Locate every blood parasite and identify its species.
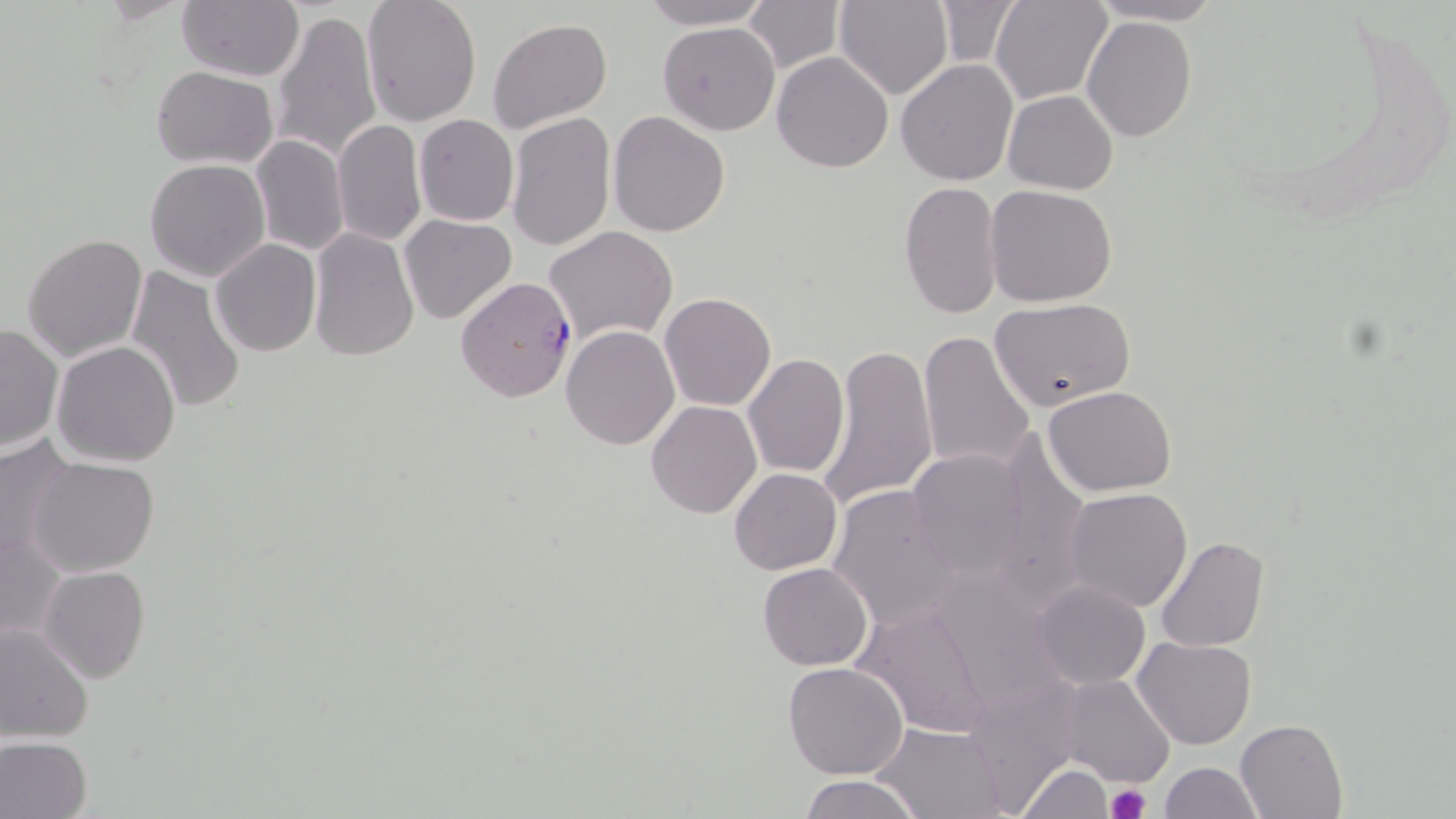
Approximate bounding boxes as (x1,y1)-(x2,y2) corner pairs in pixels.
Plasmodium falciparum-infected red blood cells: (454,276)-(579,405).
No Plasmodium ovale, Plasmodium malariae, Plasmodium vivax, Babesia divergens, or Trypanosoma brucei observed.

Uninfected red blood cell locations: (177,0)-(303,82), (360,0)-(483,127), (635,0)-(773,29), (835,0)-(953,100), (990,0)-(1111,105), (740,1)-(848,76), (934,2)-(1020,67), (1081,2)-(1233,26), (270,8)-(382,165), (1082,15)-(1198,141), (487,17)-(613,135), (658,21)-(780,134), (772,50)-(893,173), (896,59)-(1019,187), (151,66)-(277,167), (1003,90)-(1119,194), (607,111)-(731,237), (506,112)-(615,252), (414,114)-(519,226), (332,117)-(425,249), (249,135)-(349,257), (145,158)-(270,281), (899,180)-(1005,322), (984,184)-(1117,306), (399,214)-(518,325), (544,225)-(679,346), (310,226)-(419,363), (22,233)-(148,362), (209,239)-(321,356), (125,267)-(244,416), (660,291)-(776,411), (990,297)-(1136,412), (0,322)-(63,453), (561,324)-(679,449), (919,330)-(1035,475), (51,341)-(181,466), (817,341)-(938,510), (742,353)-(849,477), (1046,385)-(1176,496), (645,401)-(761,518), (993,430)-(1089,608), (0,434)-(80,566), (905,448)-(1029,581), (27,457)-(159,575), (728,467)-(843,574), (826,484)-(967,632), (1063,487)-(1193,613), (0,527)-(66,642), (1154,536)-(1270,653), (758,562)-(873,670), (39,565)-(151,685), (1031,580)-(1149,690), (854,601)-(996,741), (0,622)-(95,744), (1133,636)-(1257,749), (783,662)-(908,779), (1059,673)-(1174,787), (1236,718)-(1347,818), (872,723)-(1007,818), (0,735)-(92,819), (1159,761)-(1264,818), (1016,763)-(1116,817), (799,775)-(924,819). Platelet locations: (1105,785)-(1149,819). Slide-level diagnosis: Plasmodium falciparum. May-Grünwald-Giemsa-stained preparation. Single field of view. Light microscopy. Image is 1456×819 pixels. 1000x magnification. Thin blood film.